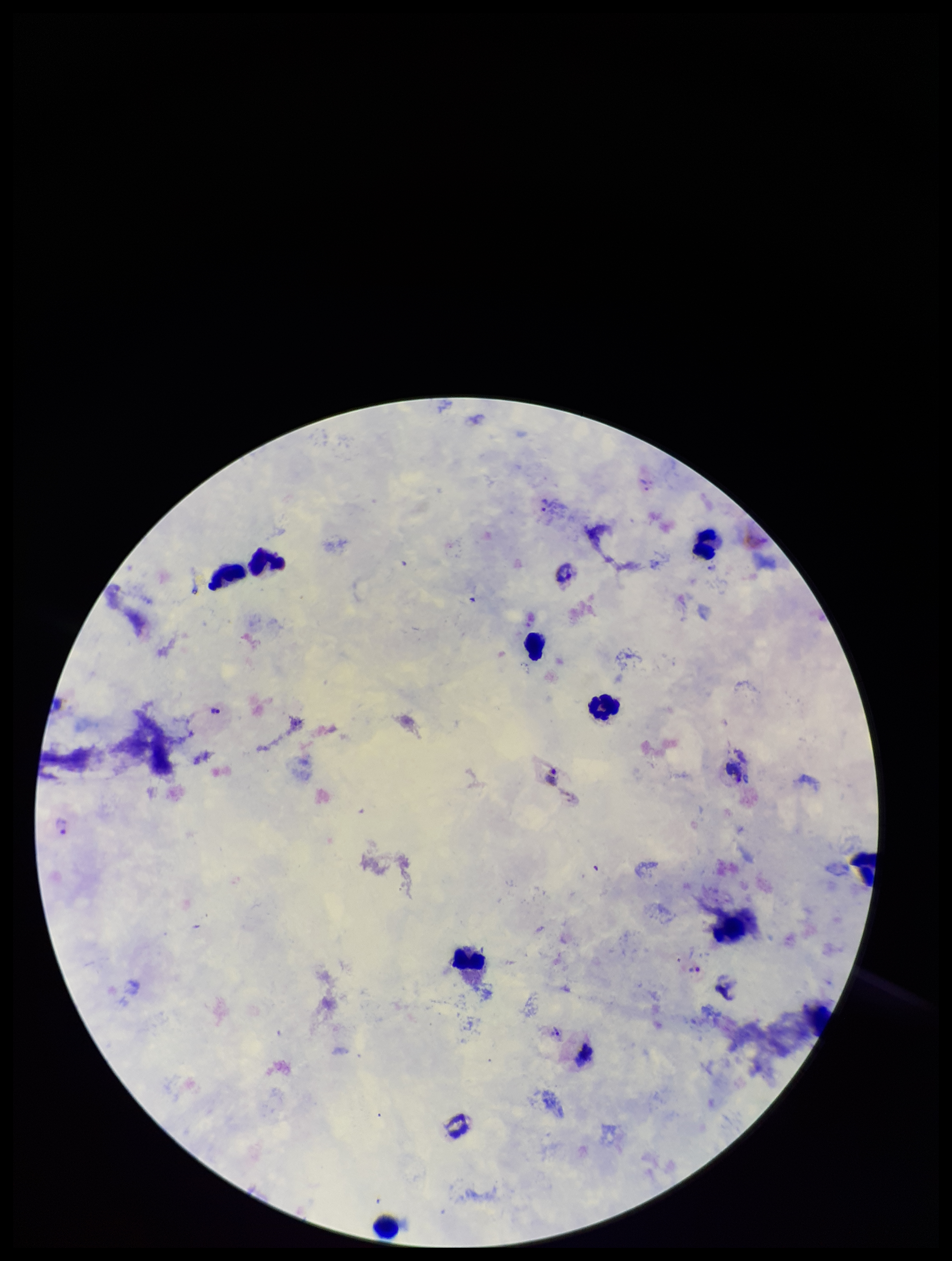
preparation: thick blood smear
patient_malaria_status: infected
field_of_view: single
leukocyte_count: 8
parasite_count: 4
image_size: 952×1261 pixels
species_reported_for_this_patient: Plasmodium vivax
capture: smartphone photograph through the microscope eyepiece
plasmodium_parasites: detected
stain: Giemsa